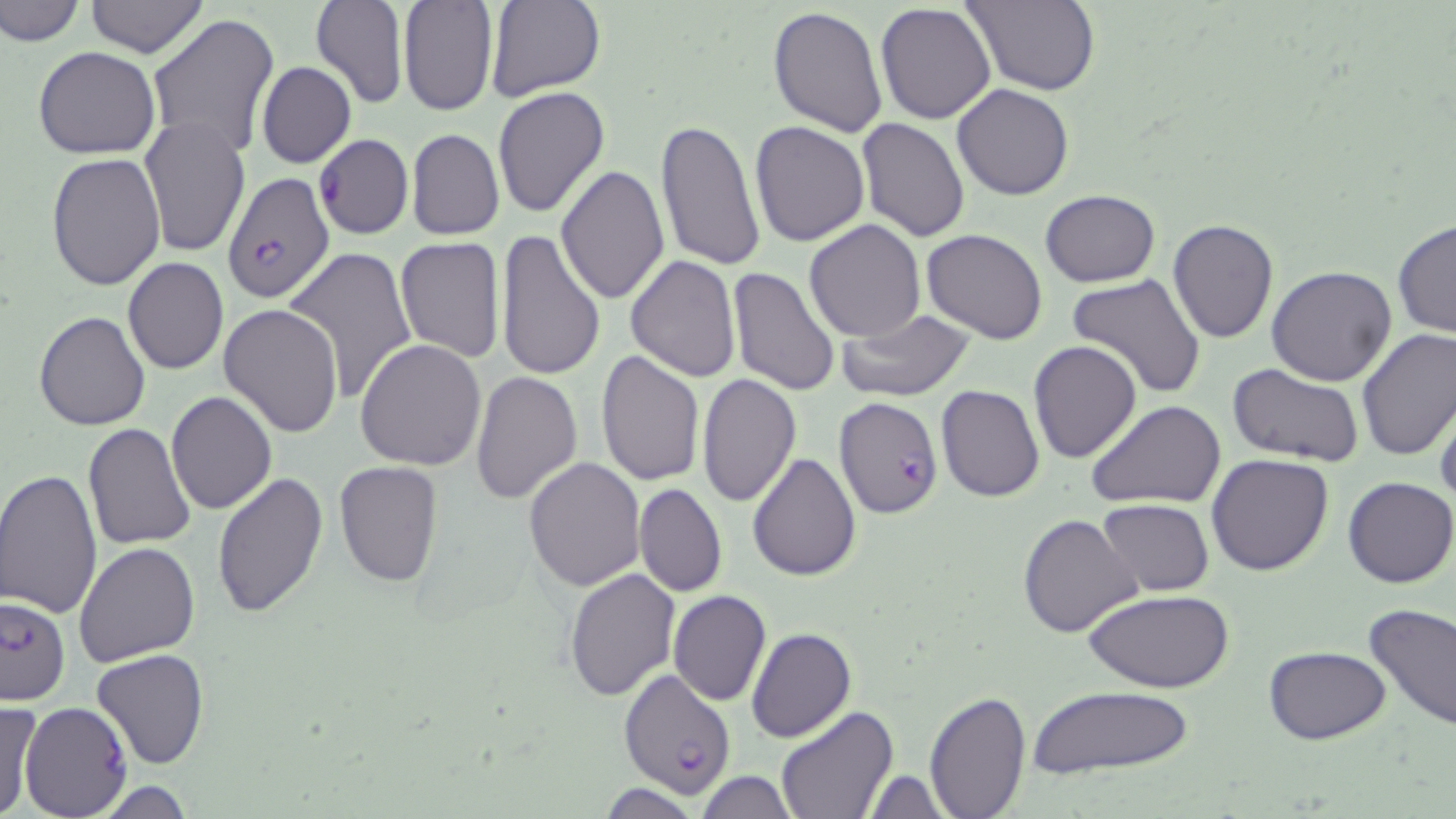

Summary:
  - Coordinate format: approximate bounding boxes as named x1/y1/x2/y2 corners in pixels
  - Uninfected red blood cell locations: (x1=0, y1=0, x2=85, y2=48), (x1=83, y1=0, x2=209, y2=58), (x1=483, y1=0, x2=605, y2=103), (x1=960, y1=0, x2=1100, y2=94), (x1=397, y1=1, x2=497, y2=116), (x1=310, y1=2, x2=409, y2=109), (x1=875, y1=3, x2=997, y2=123), (x1=768, y1=5, x2=887, y2=137), (x1=146, y1=15, x2=280, y2=163), (x1=32, y1=46, x2=160, y2=159), (x1=256, y1=62, x2=356, y2=168), (x1=952, y1=84, x2=1075, y2=200), (x1=491, y1=86, x2=610, y2=219), (x1=138, y1=115, x2=248, y2=259), (x1=655, y1=118, x2=764, y2=270), (x1=859, y1=119, x2=970, y2=243), (x1=749, y1=121, x2=869, y2=247), (x1=406, y1=127, x2=504, y2=240), (x1=313, y1=134, x2=413, y2=240), (x1=46, y1=152, x2=166, y2=292), (x1=555, y1=165, x2=669, y2=306), (x1=1039, y1=188, x2=1160, y2=287), (x1=1393, y1=217, x2=1455, y2=340), (x1=1167, y1=219, x2=1279, y2=344), (x1=804, y1=220, x2=926, y2=341), (x1=494, y1=227, x2=606, y2=383), (x1=922, y1=229, x2=1047, y2=344), (x1=395, y1=237, x2=505, y2=362), (x1=285, y1=248, x2=420, y2=404), (x1=626, y1=254, x2=742, y2=381), (x1=123, y1=257, x2=229, y2=374), (x1=726, y1=265, x2=841, y2=396), (x1=1267, y1=265, x2=1398, y2=386), (x1=1066, y1=273, x2=1206, y2=399), (x1=219, y1=302, x2=344, y2=437), (x1=838, y1=309, x2=976, y2=401), (x1=33, y1=312, x2=150, y2=431), (x1=1356, y1=328, x2=1456, y2=461), (x1=355, y1=338, x2=488, y2=470), (x1=1028, y1=339, x2=1143, y2=464), (x1=596, y1=350, x2=704, y2=487), (x1=1226, y1=365, x2=1364, y2=467), (x1=469, y1=370, x2=582, y2=506), (x1=697, y1=375, x2=801, y2=505), (x1=936, y1=385, x2=1044, y2=501), (x1=1431, y1=389, x2=1455, y2=507), (x1=167, y1=391, x2=277, y2=513), (x1=1087, y1=399, x2=1227, y2=510), (x1=82, y1=423, x2=197, y2=551), (x1=748, y1=450, x2=861, y2=580), (x1=1205, y1=453, x2=1333, y2=576), (x1=523, y1=456, x2=646, y2=591), (x1=333, y1=461, x2=443, y2=588), (x1=0, y1=468, x2=102, y2=619), (x1=210, y1=471, x2=328, y2=618), (x1=1343, y1=476, x2=1456, y2=589), (x1=633, y1=483, x2=726, y2=597), (x1=1097, y1=498, x2=1214, y2=596), (x1=1017, y1=514, x2=1145, y2=639), (x1=74, y1=540, x2=201, y2=667), (x1=565, y1=568, x2=680, y2=703), (x1=1085, y1=589, x2=1235, y2=694), (x1=667, y1=590, x2=771, y2=707), (x1=1362, y1=604, x2=1456, y2=734), (x1=745, y1=627, x2=856, y2=743), (x1=1265, y1=646, x2=1390, y2=745), (x1=92, y1=647, x2=210, y2=769), (x1=1028, y1=687, x2=1198, y2=779), (x1=923, y1=688, x2=1029, y2=818), (x1=0, y1=700, x2=40, y2=819), (x1=20, y1=702, x2=132, y2=817), (x1=774, y1=704, x2=897, y2=819), (x1=860, y1=769, x2=952, y2=818), (x1=694, y1=772, x2=801, y2=817), (x1=87, y1=777, x2=199, y2=817), (x1=596, y1=782, x2=701, y2=819)
  - Plasmodium falciparum-infected red blood cell locations: (x1=223, y1=172, x2=334, y2=303), (x1=833, y1=396, x2=944, y2=519), (x1=1, y1=596, x2=70, y2=706), (x1=620, y1=667, x2=736, y2=797)
  - Slide-level diagnosis: Plasmodium falciparum
  - Image size: 1456×819 pixels
  - Stain: May-Grünwald-Giemsa
  - Modality: light microscopy
  - Magnification: 1000x
  - Field of view: one of a larger specimen
  - Preparation: thin blood film